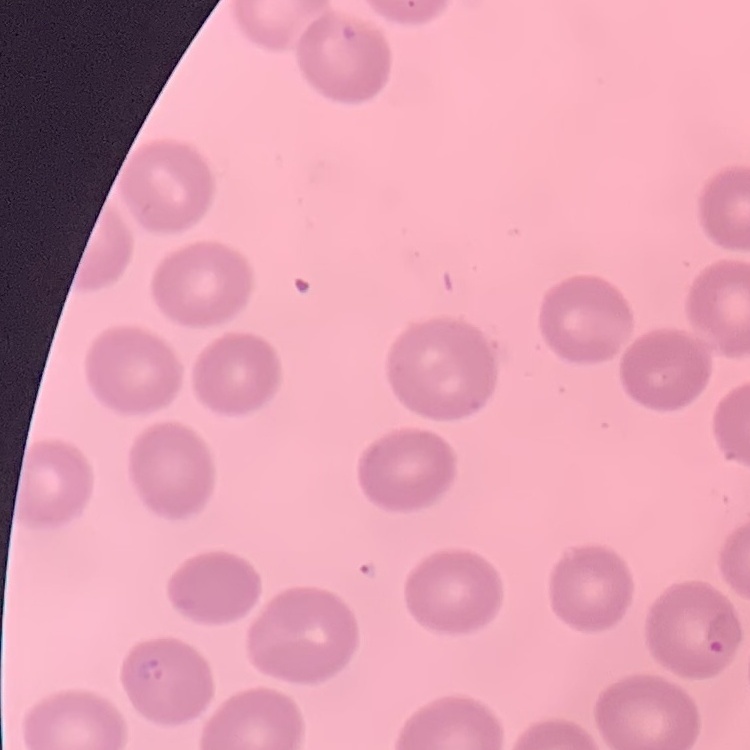 The red blood cells show no rouleaux formation. Stained with either Field's or Giemsa. Square crop of a larger photomicrograph. Thin blood smear.